Report the malaria status of this cell.
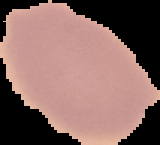

Uninfected.

Summary:
  - Preparation: thin blood film
  - Image size: 160×145 pixels
  - Image type: segmented cell region with the area outside set to black